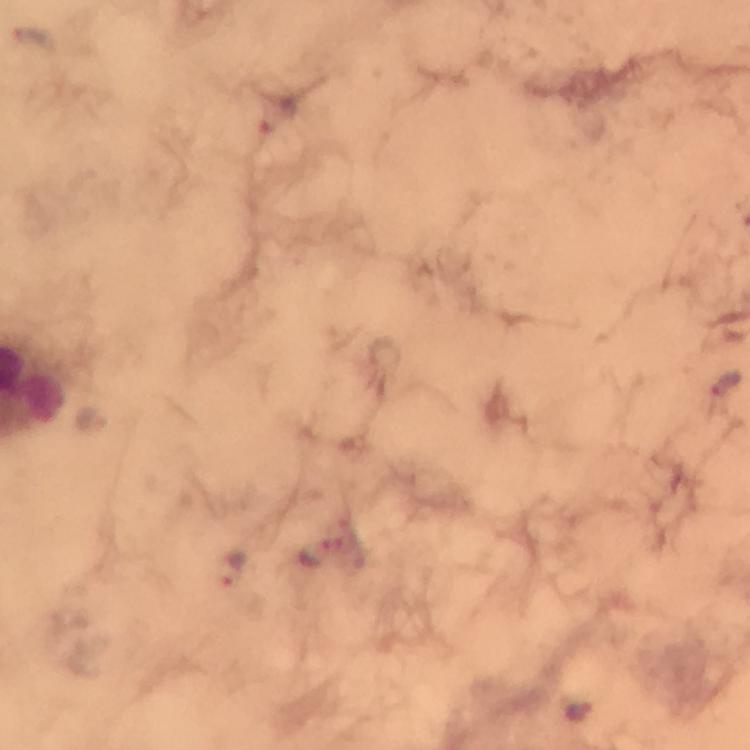

Approximate object centers, in pixels from the top-left corner. Plasmodium parasite locations: (x=725, y=383), (x=90, y=417), (x=316, y=556), (x=235, y=570), (x=576, y=711). Immersion oil was used. Cropped region of a single field of view. 100x magnification. From a malaria diagnostic workup. Giemsa-stained preparation. Thick blood smear. Smartphone photograph taken through a microscope. Image is 750×750 pixels.